Assess the morphology of the erythrocytes.
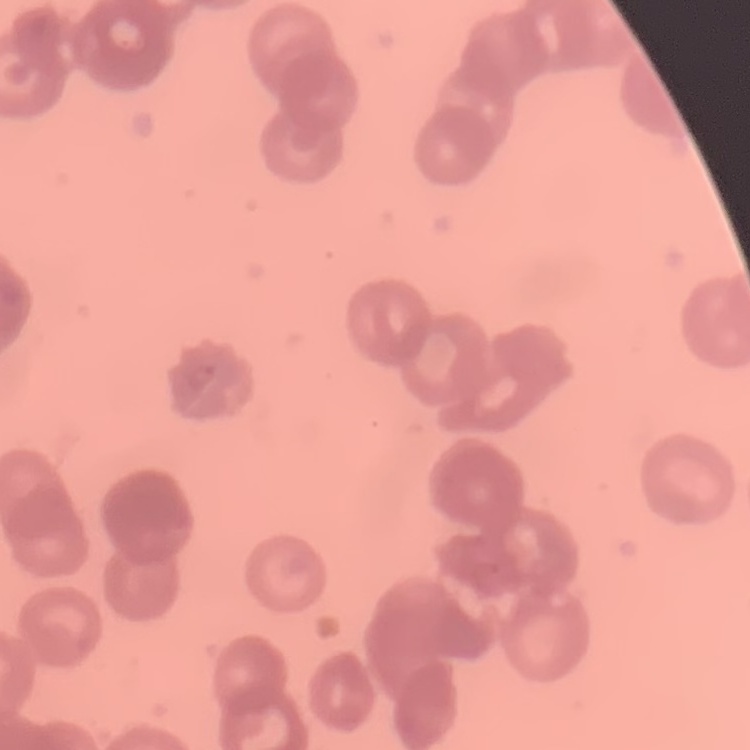
Rouleaux formation.

{
  "preparation": "thin blood smear",
  "image_type": "square crop of a larger photomicrograph",
  "stain": "Field's or Giemsa"
}